Describe the morphology of the erythrocytes.
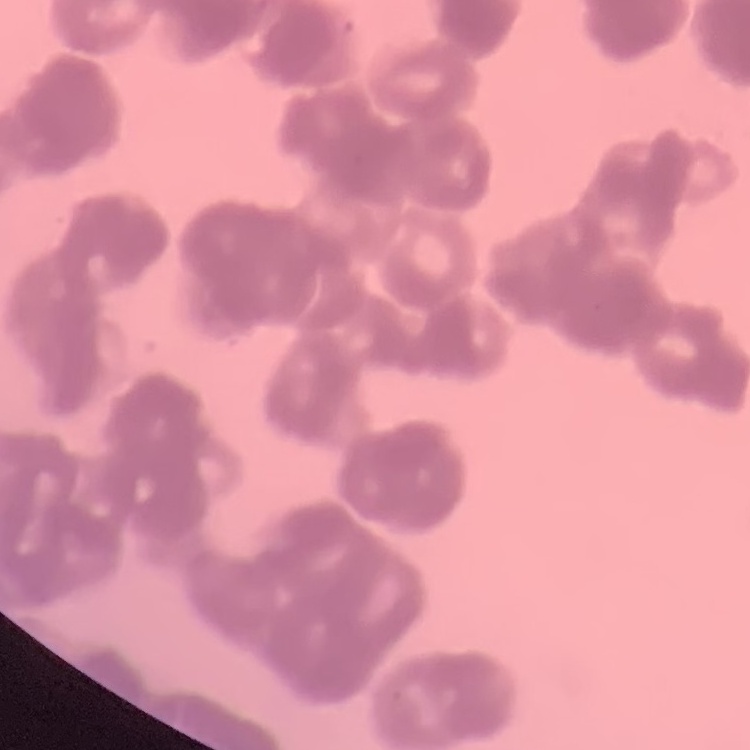
Rouleaux formation.

Summary:
  - Stain: Field's or Giemsa
  - Image type: one tile cut from a larger photomicrograph
  - Preparation: thin blood smear